Identify the parasite.
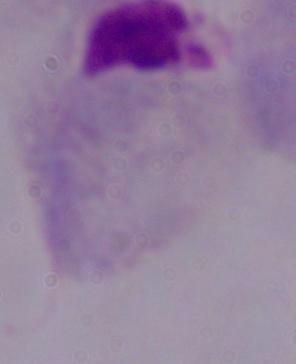

This is a trichomonad.

Summary:
  - Modality: photomicrograph
  - Magnification: 1000x